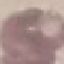
malaria status = uninfected
capture = smartphone through the microscope eyepiece
image type = automatically extracted cell patch, resized to 64 × 64 pixels
stain = Giemsa
preparation = thin smear